Assess this cell for malaria.
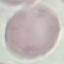
It is uninfected.

Acquired by smartphone through the microscope eyepiece. Giemsa stain. Thin smear of blood. Cell patch, automatically extracted from a larger field of view and resized to 64 × 64 pixels.